Classify this cell by malaria status.
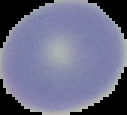
It is uninfected.

Summary:
  - Preparation: thin blood smear
  - Image type: cell region segmented out of the field of view; surrounding area masked to black
  - Image size: 127×115 pixels